Locate every malaria parasite.
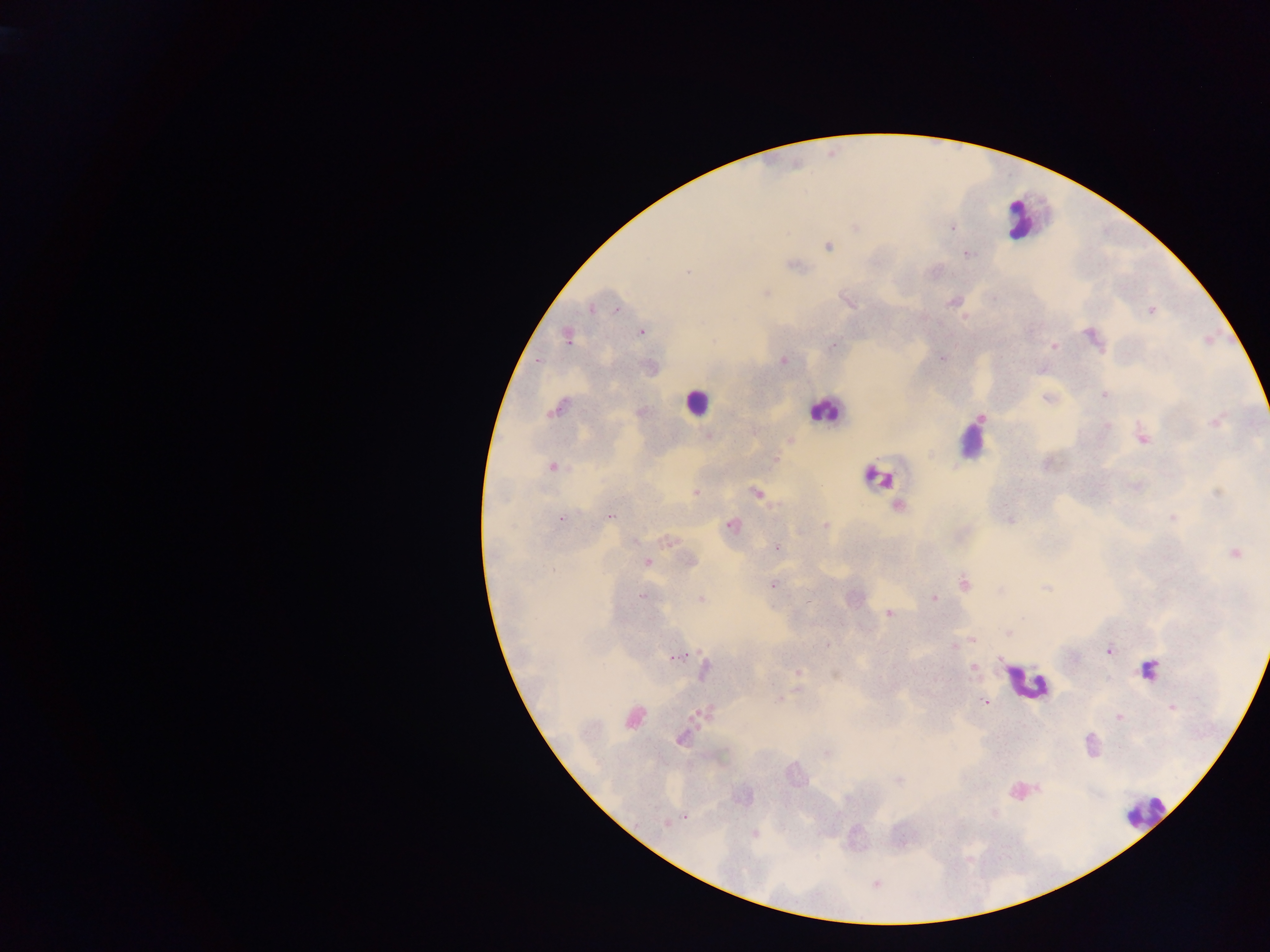
Approximate centers as (x, y) in pixels.
Malaria parasites: (855, 226), (952, 228), (828, 246), (965, 253), (792, 265), (765, 293), (954, 300), (848, 302), (592, 307), (1151, 310), (617, 311), (641, 331), (566, 336), (1093, 338), (833, 346), (1052, 346), (940, 358), (782, 360), (537, 361), (1041, 369), (1104, 393), (1048, 398), (558, 408), (639, 411), (980, 417), (1216, 421), (1105, 425), (708, 436), (1141, 437), (788, 440), (772, 459), (551, 466), (1137, 486), (695, 493), (756, 493), (1218, 493), (898, 507), (609, 517), (1172, 517), (560, 518), (1010, 519), (731, 525), (826, 526), (668, 540), (777, 548), (1233, 552), (690, 561), (646, 562), (772, 583), (964, 583), (1046, 587), (642, 596), (701, 598), (932, 598), (808, 601), (889, 613), (1007, 632), (972, 640), (826, 645), (953, 645), (1108, 650), (676, 656), (973, 667), (704, 670), (797, 672), (836, 675), (780, 698), (985, 701), (1171, 707), (703, 713), (1119, 717), (633, 718), (681, 737), (826, 753), (900, 780), (994, 812), (685, 816), (667, 822), (754, 834), (876, 882).

image size = 1270×952 pixels
country = Ghana
preparation = thick blood film
field of view = single
leukocyte locations = approximate centers as (x, y) in pixels: (1027, 218), (696, 402), (825, 409), (971, 438), (878, 477), (1147, 670), (1026, 683), (1020, 791), (1144, 810)
capture = mobile-phone photograph through a microscope